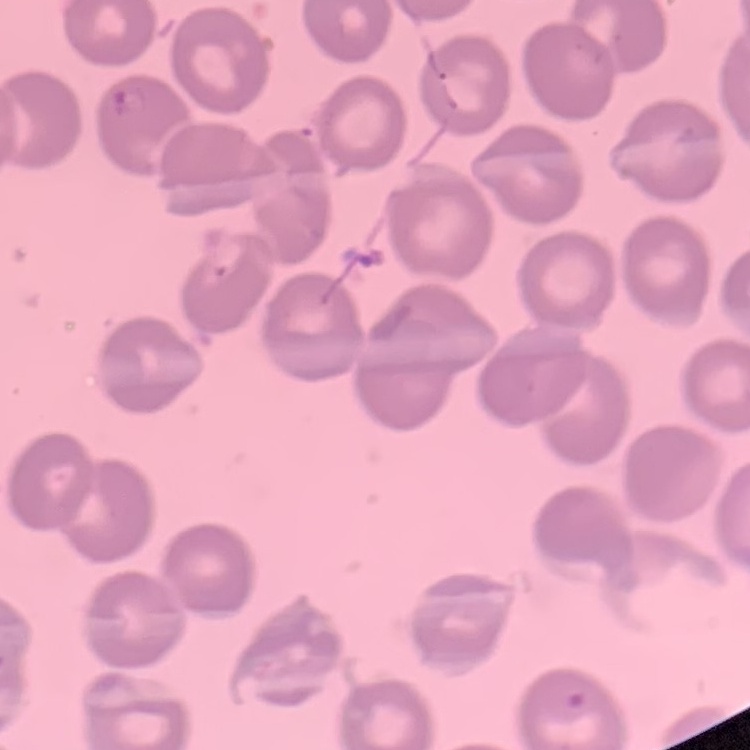
erythrocyte_morphology: no rouleaux formation
stain: Field's or Giemsa
image_type: one tile cut from a larger photomicrograph
preparation: thin blood film